Classify this cell by malaria status.
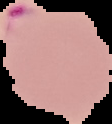

It is parasitized.

The area outside the segmented cell region is set to black. From a thin blood film. Image is 112×124 pixels.